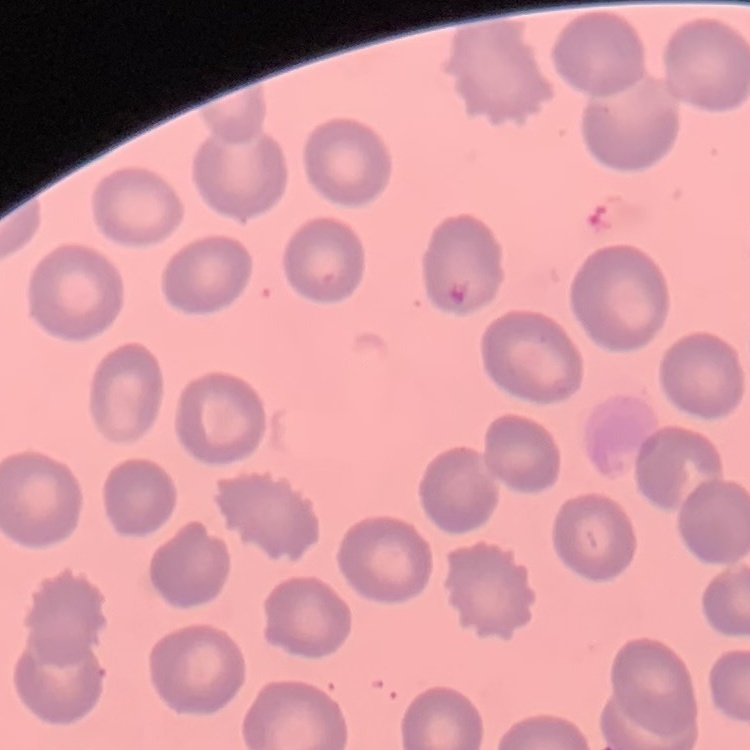

{
  "erythrocyte_morphology": "no rouleaux formation",
  "preparation": "thin blood film",
  "image_type": "one tile cut from a larger photomicrograph",
  "stain": "Field's or Giemsa"
}